Assess the morphology of the red blood cells.
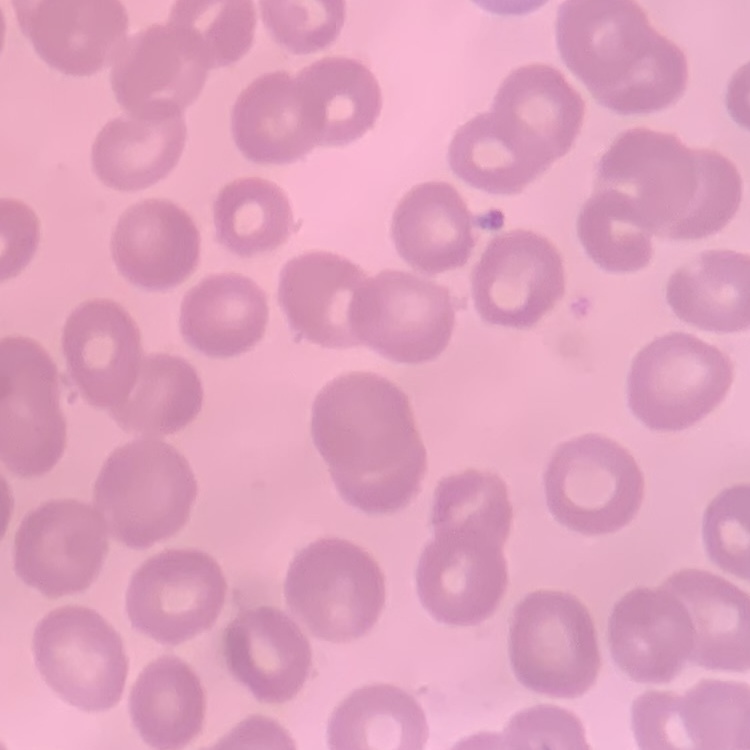
No rouleaux formation.

{
  "stain": "Field's or Giemsa",
  "preparation": "thin blood smear",
  "image_type": "one tile cut from a larger photomicrograph"
}